Classify this cell by malaria status.
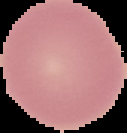

It is uninfected.

Image is 127×133 pixels. Segmented cell region on a black background. From a thin blood film.